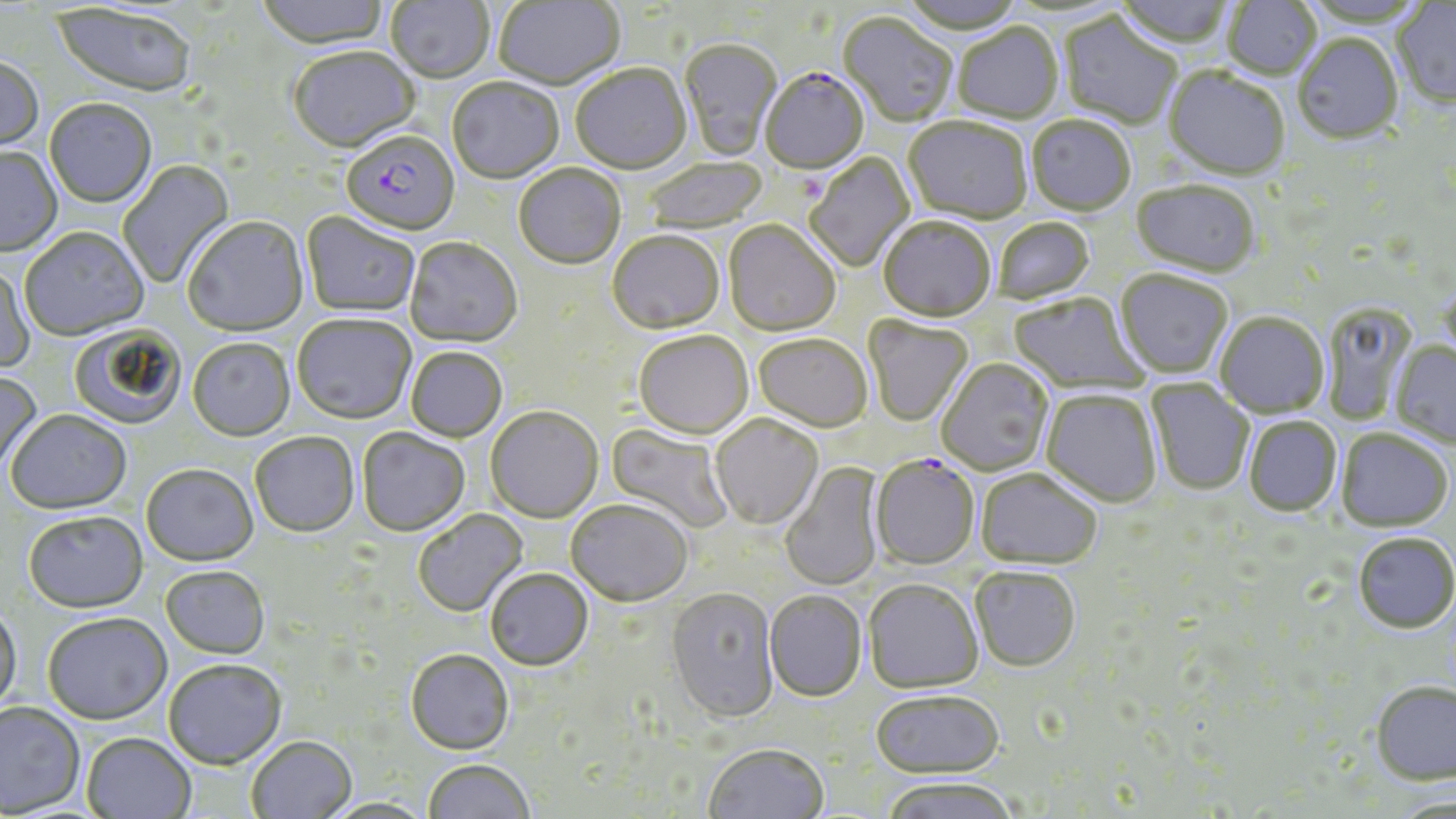

slide-level diagnosis = Plasmodium falciparum
field of view = single
modality = optical microscopy
magnification = 1000x
uninfected red blood cell locations = approximate bounding boxes as [x1, y1, x2, y2] in pixels: [256, 0, 390, 53], [385, 0, 495, 86], [896, 0, 1026, 36], [1113, 0, 1235, 51], [493, 1, 625, 91], [1222, 1, 1321, 81], [1392, 2, 1456, 110], [50, 3, 196, 101], [1058, 13, 1182, 131], [838, 14, 958, 128], [954, 25, 1063, 125], [1292, 36, 1403, 147], [679, 40, 783, 162], [288, 48, 420, 156], [0, 59, 44, 156], [570, 66, 692, 177], [1163, 68, 1290, 183], [447, 80, 564, 185], [45, 100, 156, 210], [1026, 117, 1135, 218], [903, 119, 1032, 226], [0, 149, 62, 258], [805, 153, 916, 273], [644, 158, 768, 234], [117, 159, 236, 288], [514, 166, 626, 272], [1131, 184, 1260, 279], [301, 213, 420, 319], [183, 218, 309, 338], [879, 219, 996, 325], [993, 219, 1096, 306], [723, 221, 840, 338], [20, 230, 149, 343], [607, 233, 725, 336], [405, 239, 522, 349], [0, 264, 36, 375], [1115, 270, 1233, 380], [1009, 293, 1149, 395], [1322, 302, 1418, 426], [1215, 313, 1329, 419], [293, 317, 416, 427], [862, 317, 974, 428], [69, 324, 186, 430], [633, 333, 753, 441], [753, 335, 873, 433], [187, 340, 295, 443], [1390, 342, 1456, 449], [406, 348, 507, 443], [937, 359, 1054, 477], [0, 370, 42, 476], [1146, 379, 1255, 496], [1041, 390, 1162, 508], [485, 408, 604, 524], [5, 411, 132, 516], [710, 415, 823, 530], [1244, 416, 1342, 517], [606, 423, 733, 534], [357, 429, 470, 537], [1336, 430, 1453, 532], [250, 434, 359, 539], [780, 462, 885, 591], [141, 466, 259, 568], [975, 470, 1103, 571], [565, 502, 693, 609], [414, 509, 529, 619], [22, 513, 148, 616], [1353, 533, 1455, 634], [160, 567, 270, 661], [969, 568, 1081, 673], [485, 571, 593, 673], [863, 581, 983, 695], [666, 589, 780, 726], [765, 592, 867, 704], [0, 606, 23, 718], [42, 615, 172, 727], [405, 652, 514, 757], [163, 662, 286, 771], [1369, 680, 1456, 785], [870, 692, 1005, 780], [0, 704, 85, 818], [81, 734, 196, 819], [246, 738, 357, 819], [704, 745, 829, 819], [423, 760, 534, 819], [881, 778, 1020, 819], [319, 798, 437, 819]
Plasmodium falciparum-infected red blood cell locations = approximate bounding boxes as [x1, y1, x2, y2] in pixels: [761, 70, 869, 176], [341, 133, 459, 239], [870, 457, 979, 572]
preparation = thin blood smear
stain = May-Grünwald-Giemsa
image size = 1456×819 pixels